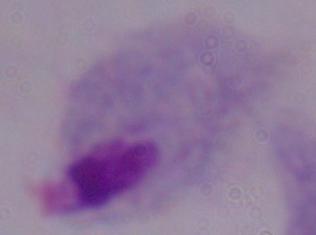

Summary:
  - Magnification: 1000x
  - Identification: trichomonad
  - Modality: photomicrograph